Assess the morphology of the erythrocytes.
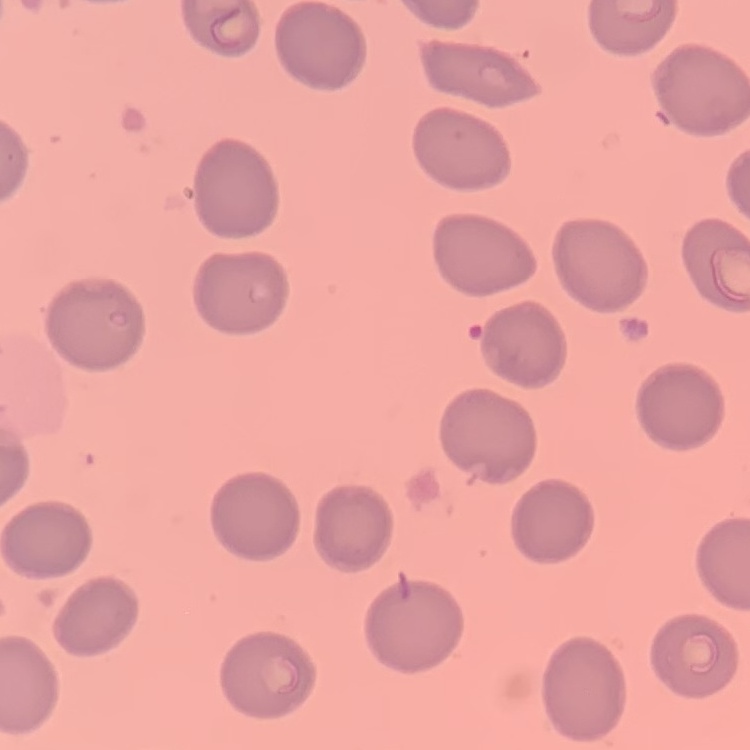

They show no rouleaux formation.

Summary:
  - Image type: one tile cut from a larger photomicrograph
  - Stain: Field's or Giemsa
  - Preparation: thin blood film